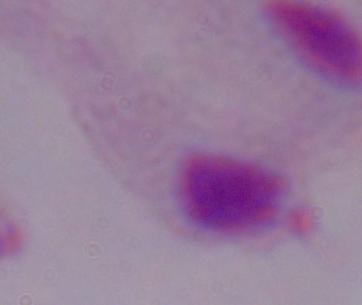

{
  "identification": "trichomonad",
  "modality": "photomicrograph",
  "magnification": "1000x"
}